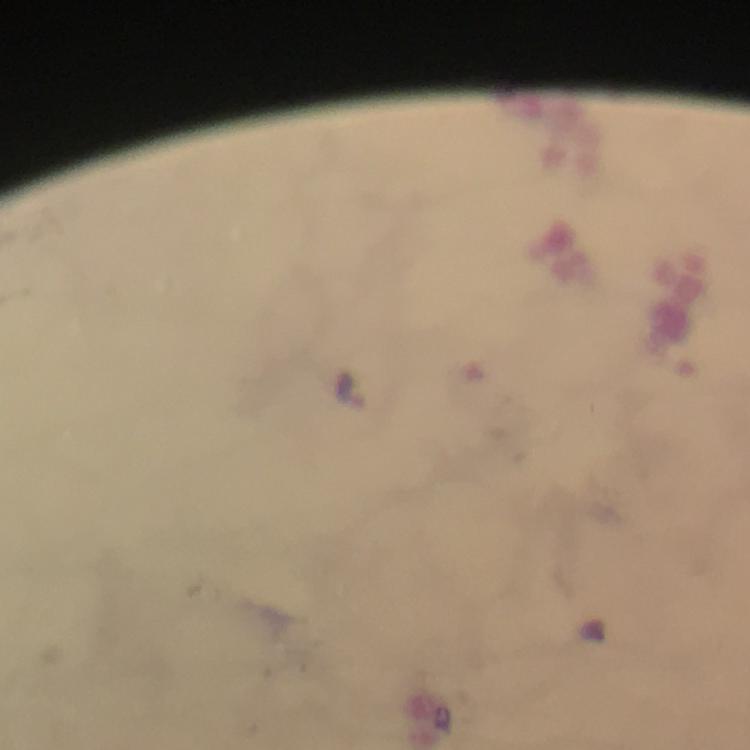

stain = Giemsa
context = from a malaria diagnostic workup
image size = 750×750 pixels
magnification = 100x
malaria parasite locations = approximate centers as {x, y} in pixels: {348, 388}
capture = smartphone mounted on the microscope
cropped from = one field of view
immersion oil = used
preparation = thick blood film